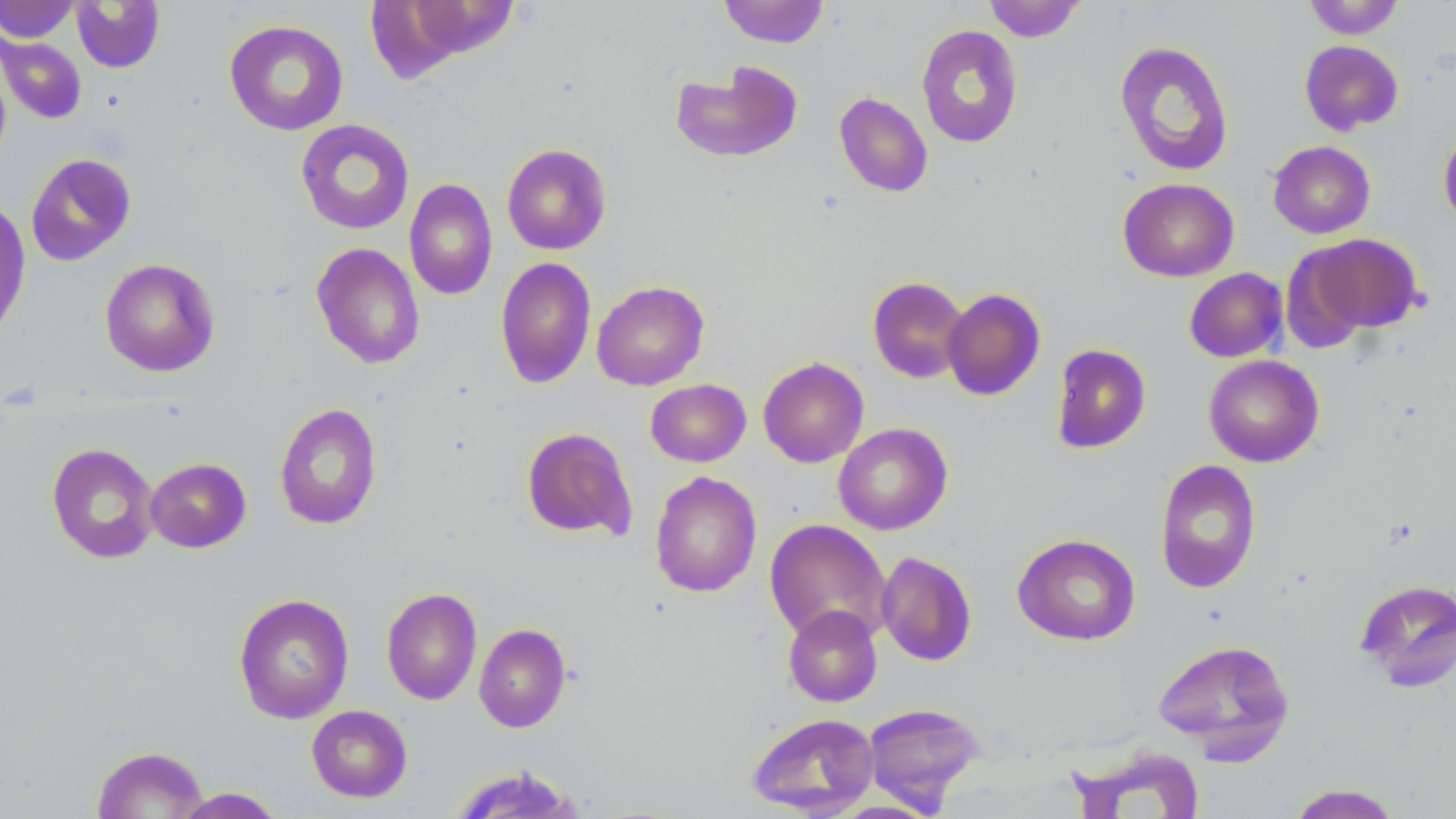

Approximate bounding boxes as named x1/y1/x2/y2 corners in pixels. Uninfected red blood cell locations: (x1=0, y1=0, x2=80, y2=43), (x1=719, y1=0, x2=829, y2=47), (x1=984, y1=0, x2=1086, y2=42), (x1=1302, y1=0, x2=1405, y2=39), (x1=71, y1=1, x2=165, y2=73), (x1=224, y1=19, x2=349, y2=135), (x1=916, y1=24, x2=1023, y2=148), (x1=1, y1=35, x2=87, y2=124), (x1=1114, y1=40, x2=1235, y2=177), (x1=1299, y1=40, x2=1404, y2=136), (x1=670, y1=60, x2=804, y2=163), (x1=834, y1=91, x2=933, y2=197), (x1=295, y1=119, x2=415, y2=235), (x1=1438, y1=125, x2=1456, y2=230), (x1=1268, y1=141, x2=1375, y2=238), (x1=502, y1=143, x2=612, y2=255), (x1=25, y1=152, x2=137, y2=266), (x1=404, y1=178, x2=497, y2=300), (x1=1117, y1=178, x2=1239, y2=282), (x1=0, y1=197, x2=31, y2=343), (x1=1294, y1=233, x2=1425, y2=338), (x1=311, y1=242, x2=425, y2=369), (x1=495, y1=257, x2=597, y2=388), (x1=100, y1=258, x2=220, y2=377), (x1=1184, y1=268, x2=1288, y2=363), (x1=868, y1=276, x2=969, y2=383), (x1=591, y1=280, x2=709, y2=390), (x1=942, y1=287, x2=1046, y2=401), (x1=1050, y1=343, x2=1151, y2=454), (x1=1203, y1=354, x2=1324, y2=467), (x1=757, y1=357, x2=869, y2=467), (x1=646, y1=379, x2=751, y2=467), (x1=274, y1=402, x2=383, y2=530), (x1=833, y1=422, x2=953, y2=535), (x1=521, y1=427, x2=637, y2=542), (x1=46, y1=443, x2=160, y2=564), (x1=145, y1=457, x2=251, y2=553), (x1=1154, y1=459, x2=1261, y2=593), (x1=649, y1=471, x2=762, y2=597), (x1=764, y1=519, x2=892, y2=644), (x1=1012, y1=533, x2=1141, y2=645), (x1=876, y1=550, x2=977, y2=666), (x1=1354, y1=578, x2=1456, y2=692), (x1=381, y1=587, x2=482, y2=706), (x1=234, y1=593, x2=355, y2=724), (x1=783, y1=604, x2=882, y2=706), (x1=474, y1=623, x2=571, y2=732), (x1=1152, y1=638, x2=1295, y2=761), (x1=863, y1=702, x2=985, y2=809), (x1=306, y1=705, x2=413, y2=802), (x1=745, y1=712, x2=880, y2=817), (x1=92, y1=745, x2=208, y2=819), (x1=1067, y1=745, x2=1203, y2=818), (x1=448, y1=766, x2=584, y2=819), (x1=1287, y1=783, x2=1403, y2=818), (x1=170, y1=787, x2=285, y2=818). Slide-level diagnosis: negative for blood parasites. 1000x magnification. May-Grünwald-Giemsa stain. Image is 1456×819 pixels. Light microscopy. Thin blood smear. Single field of view.